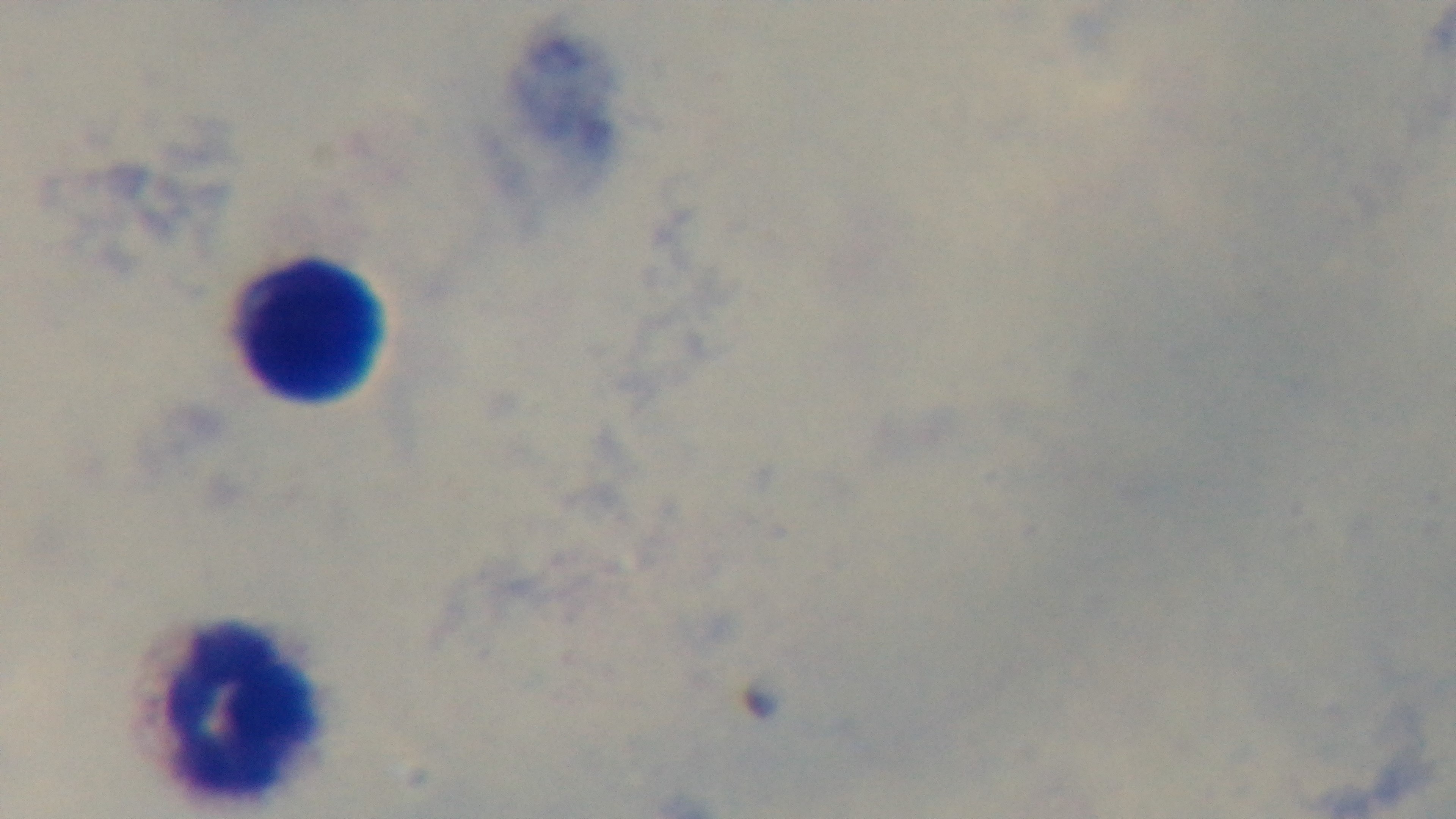
capture = mounted 4K digital camera
modality = light microscopy
preparation = thick
objective = 100x oil immersion
stain = Giemsa
field of view = single
malaria status = negative